Identify the cell.
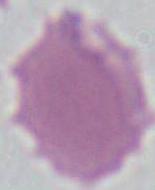

This is an erythrocyte.

Summary:
  - Modality: photomicrograph
  - Magnification: 1000x